Classify this cell by malaria status.
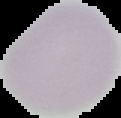

It is uninfected.

From a thin blood smear. Image is 121×118 pixels. Cell region segmented out of the field of view; the surrounding area is masked to black.